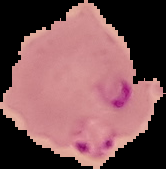

Summary:
  - Image type: segmented cell region on a black background
  - Preparation: thin blood smear
  - Image size: 166×169 pixels
  - Result: malaria parasites detected